Report the malaria status of this cell.
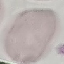

Uninfected.

Giemsa stain. Thin blood smear. Cell patch, automatically extracted from a larger field of view and resized to 64 × 64 pixels. Photographed with a smartphone camera at the microscope eyepiece.